Outline each uninfected red blood cell.
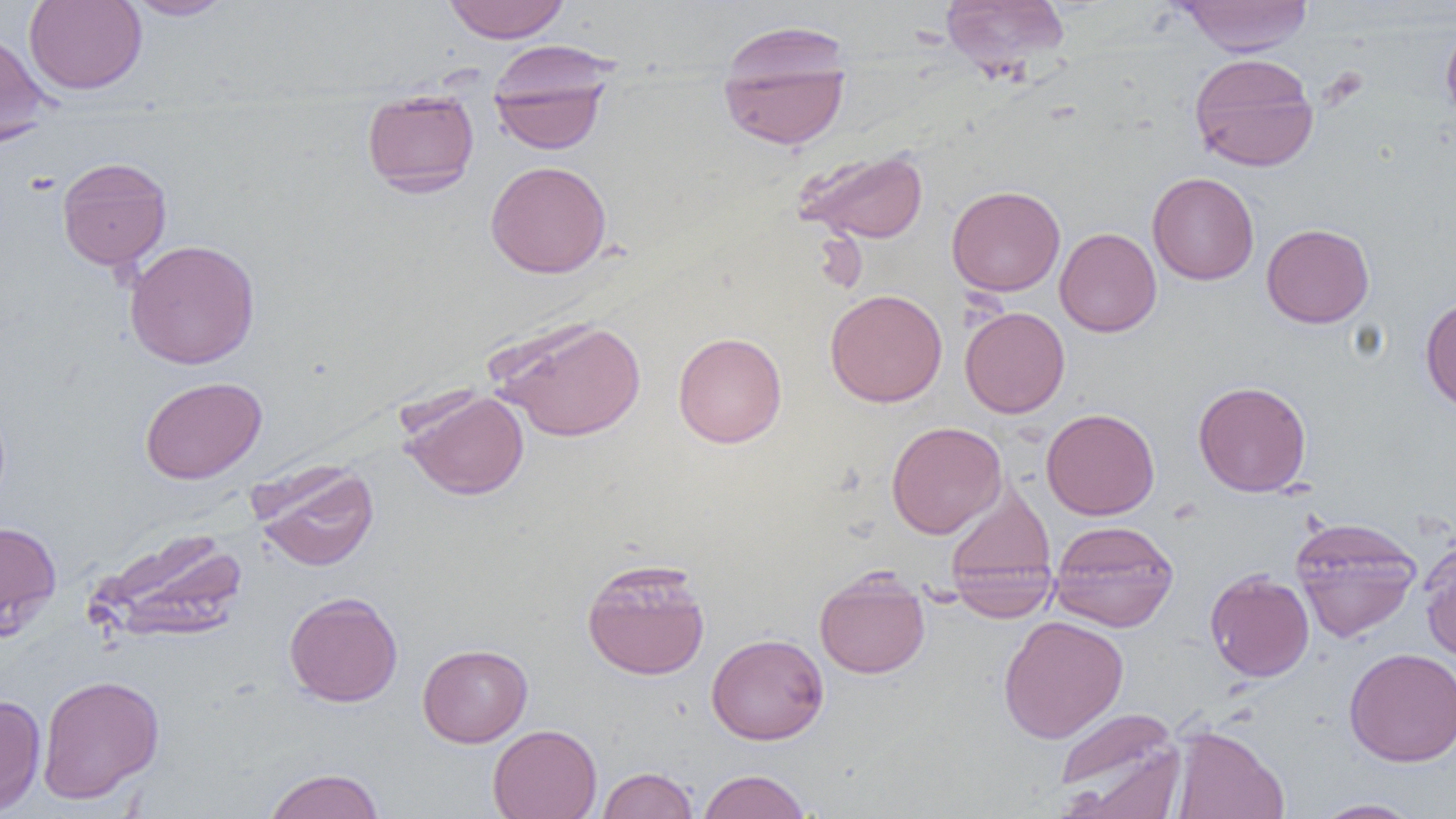

Approximate bounding boxes as (x1, y1, x2, y2) in pixels.
Uninfected red blood cells: (24, 0, 147, 94), (123, 0, 235, 20), (442, 0, 571, 43), (940, 0, 1070, 81), (1175, 0, 1313, 57), (1441, 22, 1456, 126), (716, 27, 851, 152), (0, 28, 51, 146), (489, 48, 614, 155), (1188, 53, 1319, 172), (362, 90, 480, 197), (794, 148, 929, 244), (57, 157, 172, 271), (485, 160, 612, 279), (1147, 172, 1259, 285), (946, 185, 1066, 296), (1261, 223, 1375, 328), (1055, 227, 1162, 337), (124, 239, 260, 369), (824, 289, 947, 407), (1420, 297, 1456, 414), (960, 307, 1070, 418), (487, 315, 647, 442), (673, 332, 787, 448), (139, 376, 266, 484), (1192, 381, 1312, 496), (399, 387, 530, 500), (1041, 408, 1159, 520), (886, 421, 1006, 539), (252, 462, 379, 572), (945, 481, 1057, 606), (1290, 516, 1423, 642), (0, 520, 62, 639), (1049, 520, 1179, 632), (88, 526, 248, 644), (1420, 538, 1456, 665), (949, 557, 1058, 622), (581, 558, 711, 680), (1204, 569, 1315, 682), (814, 570, 930, 679), (284, 591, 403, 707), (998, 615, 1129, 743), (706, 633, 829, 744), (417, 643, 533, 747), (1343, 647, 1456, 767), (37, 674, 165, 803), (0, 694, 47, 815), (1052, 709, 1185, 817), (487, 724, 602, 819), (1170, 725, 1289, 819), (597, 766, 699, 819), (261, 768, 386, 819), (696, 769, 812, 819), (1311, 798, 1425, 818).

Summary:
  - Slide-level diagnosis: no evidence of blood parasites
  - Magnification: 1000x
  - Image size: 1456×819 pixels
  - Modality: optical microscopy
  - Field of view: one of a larger specimen
  - Preparation: thin blood film